Classify this cell by malaria status.
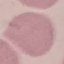

It is uninfected.

Acquired by smartphone through the microscope eyepiece. Thin blood film. Automatically extracted cell patch, resized to 64 × 64 pixels. Giemsa-stained preparation.